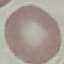
Result: no malaria parasites seen. Acquired by smartphone through the microscope eyepiece. Giemsa-stained preparation. Thin blood film. Automatically extracted cell patch, resized to 64 × 64 pixels.